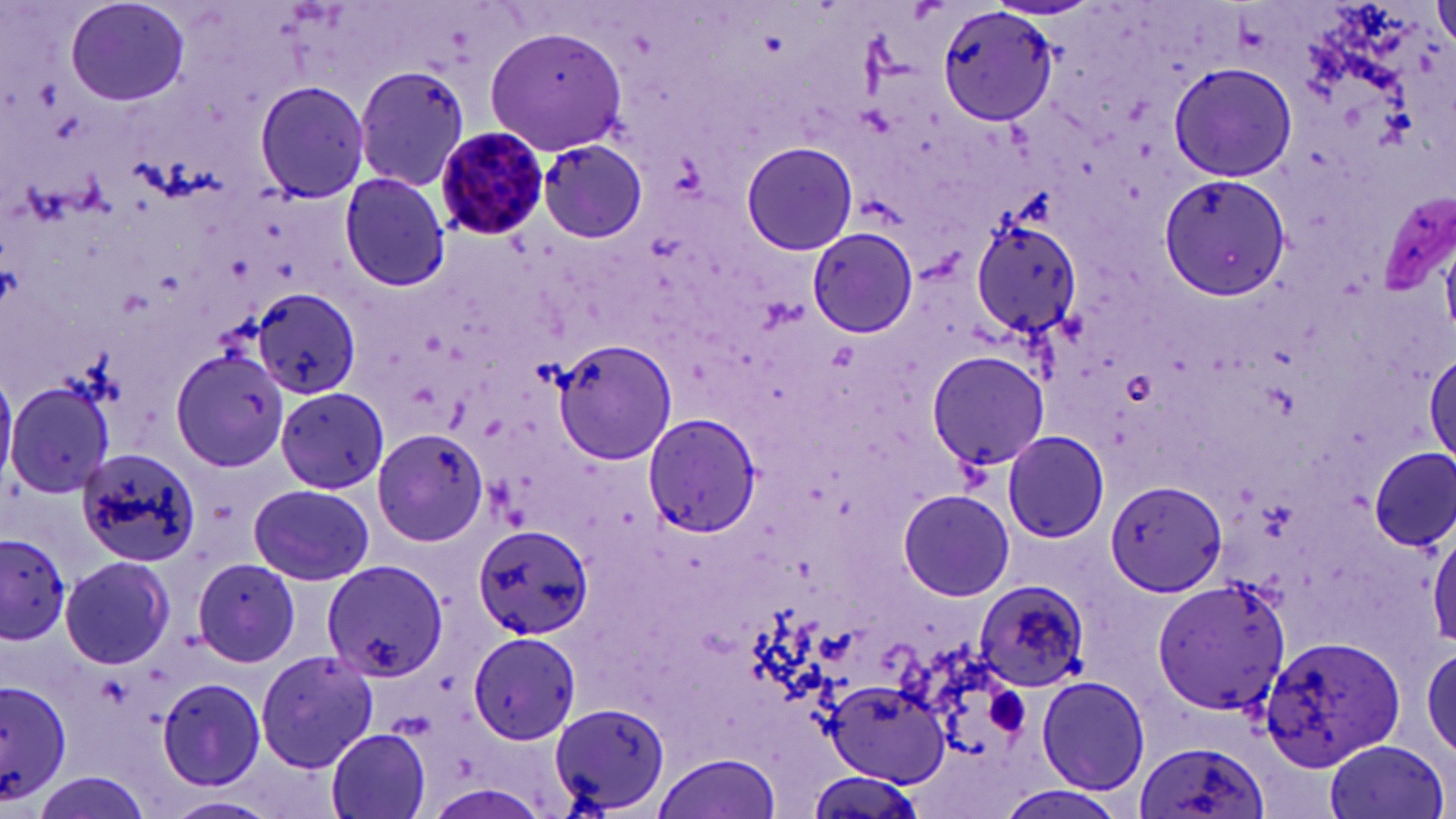 Approximate bounding boxes as (x1, y1, x2, y2) in pixels. Plasmodium malariae-infected red blood cell locations: (433, 124, 553, 241). Uninfected red blood cell locations: (1432, 1, 1456, 50), (65, 2, 191, 107), (937, 6, 1057, 127), (488, 24, 626, 153), (1169, 62, 1296, 182), (354, 64, 472, 191), (354, 65, 468, 193), (255, 79, 370, 203), (537, 140, 647, 242), (741, 141, 858, 257), (339, 172, 450, 293), (1160, 173, 1290, 301), (973, 217, 1082, 336), (808, 226, 918, 339), (811, 231, 916, 337), (253, 288, 361, 399), (553, 339, 675, 465), (1426, 349, 1456, 465), (171, 350, 290, 472), (926, 350, 1051, 471), (5, 381, 113, 498), (278, 386, 391, 493), (642, 413, 760, 539), (373, 429, 489, 545), (1002, 431, 1111, 542), (1371, 447, 1455, 551), (74, 448, 201, 567), (1105, 479, 1225, 599), (249, 483, 373, 585), (897, 488, 1015, 601), (471, 521, 593, 642), (1429, 524, 1456, 649), (0, 532, 71, 645), (61, 555, 176, 670), (195, 557, 303, 666), (324, 560, 447, 681), (973, 578, 1090, 693), (1151, 582, 1288, 719), (467, 633, 584, 745), (1259, 634, 1404, 770), (1420, 645, 1456, 761), (255, 651, 377, 772), (156, 677, 265, 790), (1036, 677, 1149, 794), (827, 681, 949, 783), (0, 682, 75, 805), (550, 706, 671, 813), (323, 726, 433, 819), (1135, 739, 1271, 819), (1324, 739, 1449, 819), (652, 752, 783, 819), (28, 772, 153, 819), (993, 782, 1131, 819), (164, 794, 280, 819). Platelet locations: (984, 687, 1032, 739). Slide-level diagnosis: Plasmodium malariae. Image is 1456×819 pixels. Thin blood smear. Optical microscopy. Captured at 1000x magnification. May-Grünwald-Giemsa stain. Single field of view.